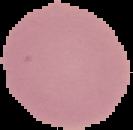

image type = segmented cell region on a black background
result = no malaria parasites detected
image size = 133×130 pixels
preparation = thin blood film